Locate every Plasmodium parasite.
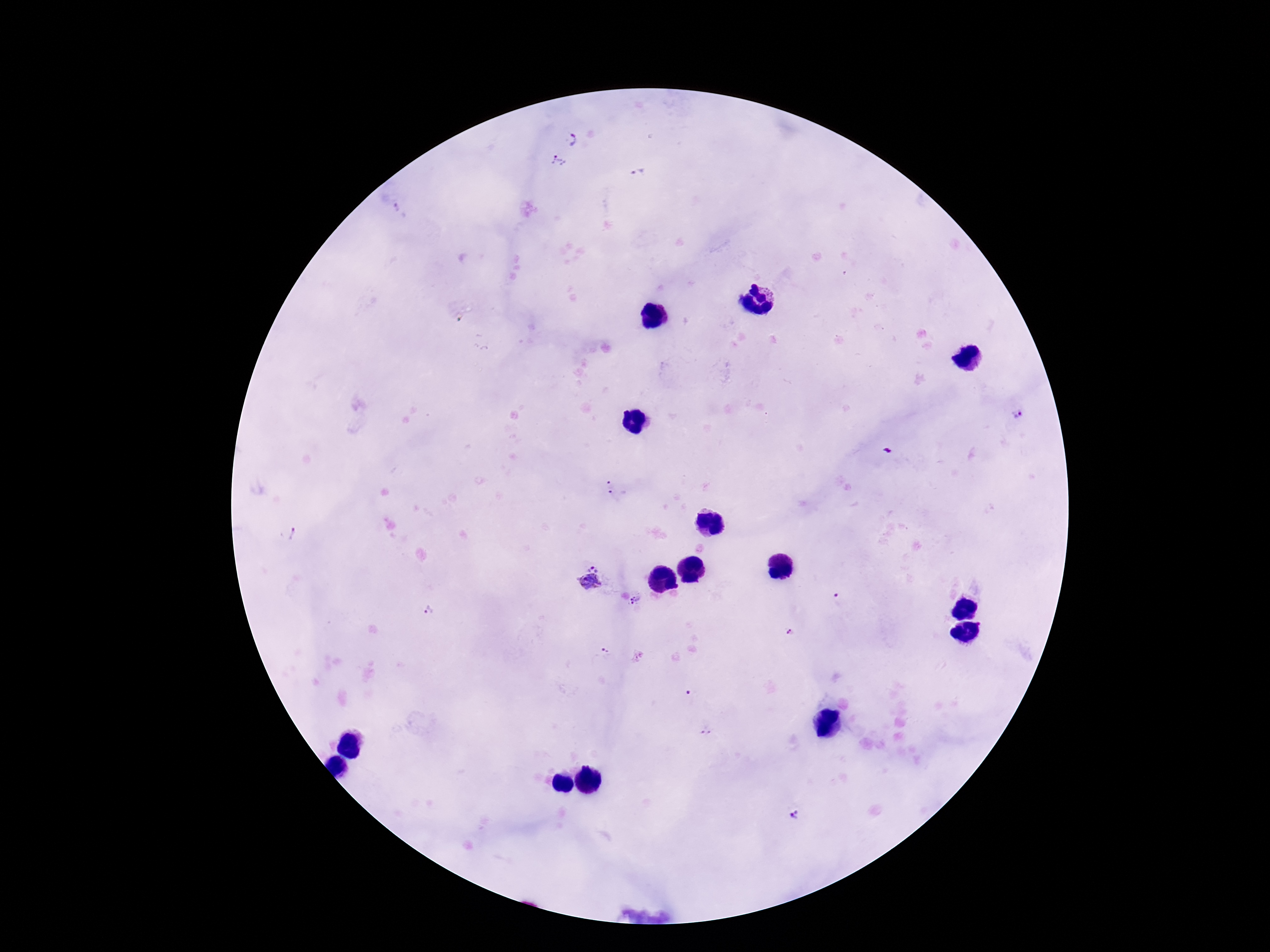

Approximate centers as (x, y) in pixels.
Plasmodium parasites: (573, 139), (556, 163), (400, 211), (1017, 414), (610, 490), (294, 536), (593, 567), (589, 585), (637, 600), (838, 600), (429, 611), (788, 633), (606, 654), (708, 729), (796, 814).

patient malaria status = infected
preparation = thick peripheral-blood smear
capture = smartphone camera through the microscope eyepiece
field of view = one from this slide
stain = Giemsa
magnification = 100x
image size = 1270×952 pixels